Mark where Plasmodium parasites and white blood cells are.
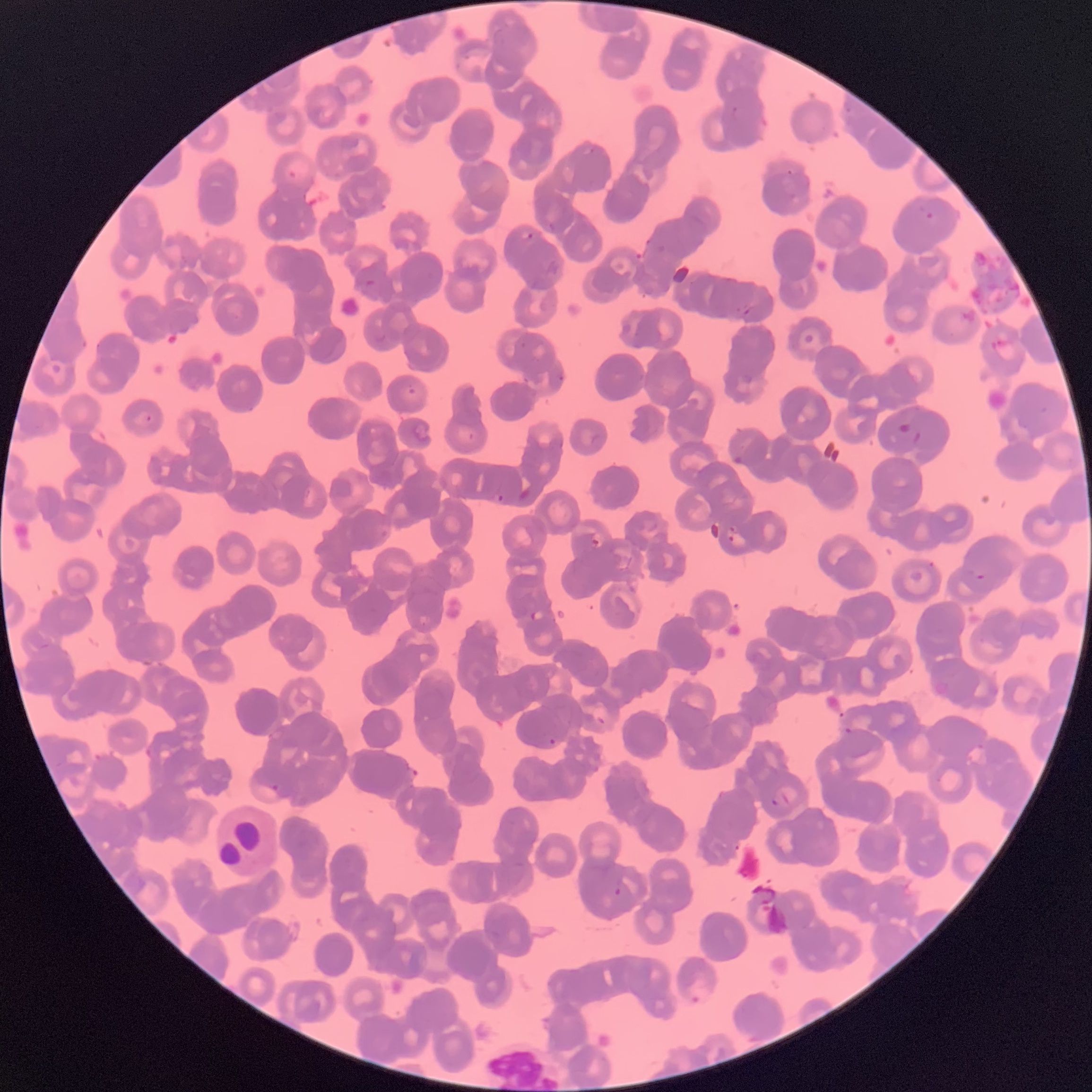
Approximate bounding boxes as [x1, y1, x2, y2] in pixels.
Plasmodium parasites: [918, 199, 947, 222], [520, 231, 535, 242], [557, 374, 565, 383], [145, 414, 153, 423], [897, 421, 924, 445], [495, 493, 506, 504], [726, 525, 738, 543], [590, 538, 600, 548], [974, 573, 988, 582], [530, 610, 544, 622], [843, 727, 854, 735], [548, 738, 556, 745], [973, 743, 987, 751], [268, 784, 282, 792], [771, 792, 790, 807], [612, 886, 622, 897], [689, 993, 703, 1007].
White blood cells: [213, 803, 281, 880].

Summary:
  - Preparation: thin blood film
  - Red blood cell morphology: rouleaux formation
  - Image size: 1092×1092 pixels
  - Modality: light microscopy